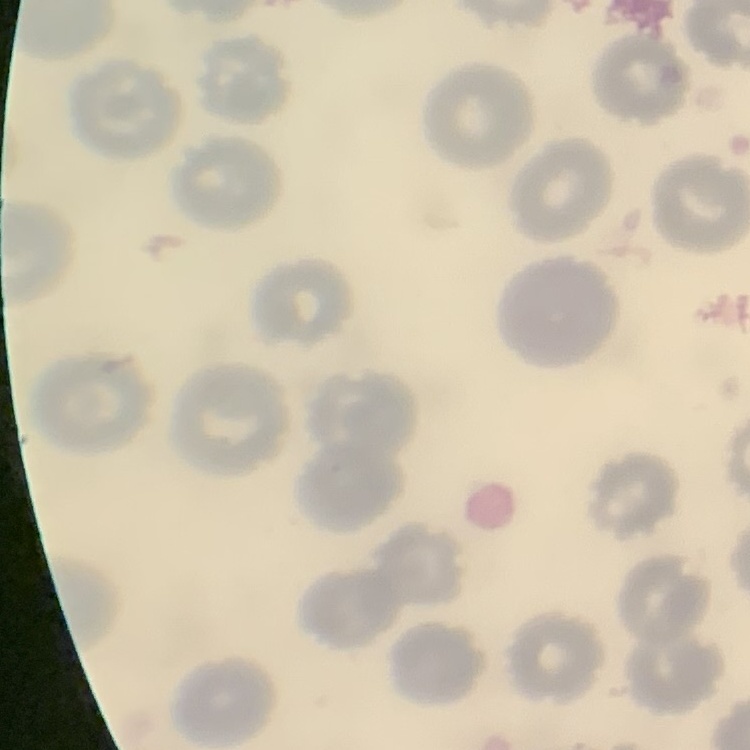
red blood cell morphology = no rouleaux formation
stain = Field's or Giemsa
preparation = thin blood film
image type = square crop of a larger photomicrograph